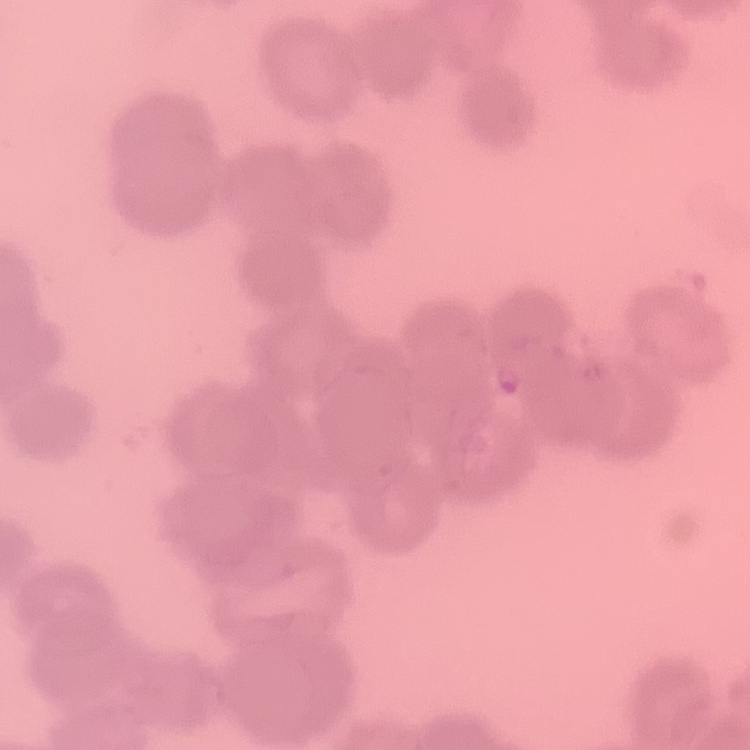
Summary:
  - Red blood cell morphology: rouleaux formation
  - Preparation: thin blood film
  - Stain: Field's or Giemsa
  - Image type: square crop of a larger photomicrograph